Classify this cell by malaria status.
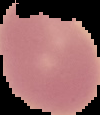

Uninfected.

preparation: thin blood smear
image_size: 100×115 pixels
image_type: segmented cell region on a black background